Report the malaria status of this cell.
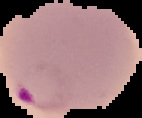
Parasitized.

image type = segmented cell region on a black background
preparation = thin blood smear
image size = 142×118 pixels